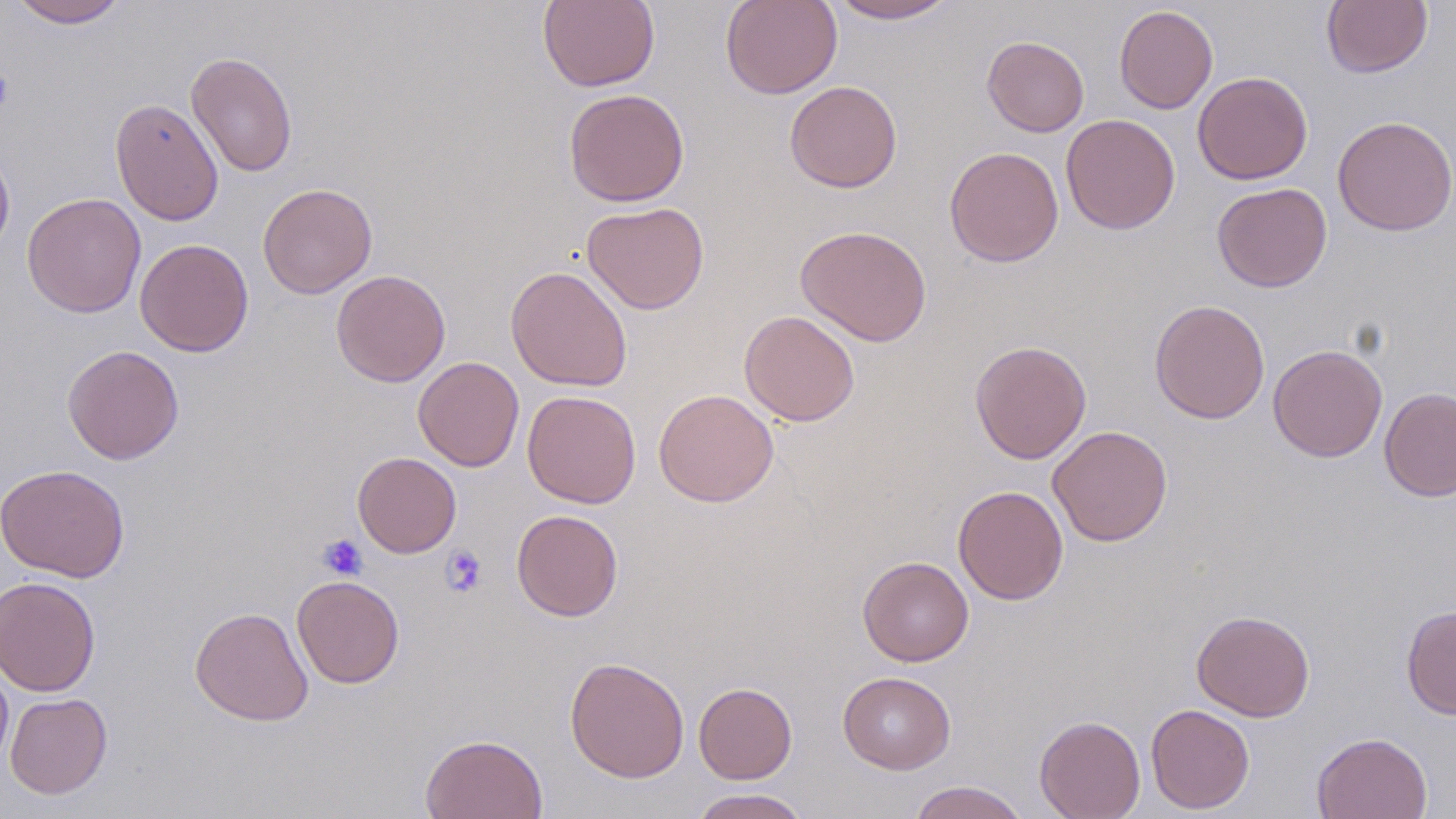

Summary:
  - Coordinate format: approximate bounding boxes as (x1, y1, x2, y2) in pixels
  - Uninfected red blood cell locations: (9, 0, 128, 28), (538, 0, 660, 92), (721, 0, 842, 99), (826, 0, 961, 24), (1322, 0, 1432, 78), (1114, 5, 1218, 114), (982, 35, 1089, 136), (186, 50, 298, 178), (1192, 71, 1313, 185), (784, 80, 902, 192), (564, 88, 689, 207), (110, 97, 224, 226), (1060, 114, 1180, 234), (1332, 115, 1456, 236), (0, 144, 15, 262), (944, 146, 1064, 268), (1212, 182, 1332, 292), (258, 183, 377, 299), (22, 193, 147, 318), (582, 201, 709, 315), (795, 225, 932, 346), (136, 239, 254, 357), (505, 265, 633, 392), (331, 269, 450, 387), (1149, 299, 1270, 424), (739, 310, 860, 427), (969, 339, 1092, 464), (61, 344, 184, 465), (1268, 344, 1388, 462), (413, 356, 524, 472), (1379, 387, 1456, 501), (653, 388, 779, 507), (522, 390, 641, 508), (1047, 425, 1172, 546), (352, 452, 461, 558), (0, 464, 130, 583), (953, 485, 1068, 605), (511, 509, 623, 621), (858, 555, 974, 666), (1, 575, 101, 697), (292, 575, 405, 688), (1401, 604, 1456, 719), (189, 606, 314, 726), (1191, 609, 1315, 722), (564, 657, 689, 782), (0, 660, 13, 776), (837, 671, 956, 774), (694, 682, 796, 784), (5, 692, 112, 799), (1145, 704, 1255, 814), (1034, 715, 1146, 819), (1312, 731, 1432, 819), (420, 733, 548, 819), (908, 780, 1030, 819), (690, 789, 807, 819)
  - Platelet locations: (0, 69, 14, 113), (318, 534, 368, 580), (440, 545, 487, 597)
  - Slide-level diagnosis: negative for blood parasites
  - Modality: light microscopy
  - Stain: May-Grünwald-Giemsa
  - Field of view: single
  - Magnification: 1000x
  - Image size: 1456×819 pixels
  - Preparation: thin blood smear